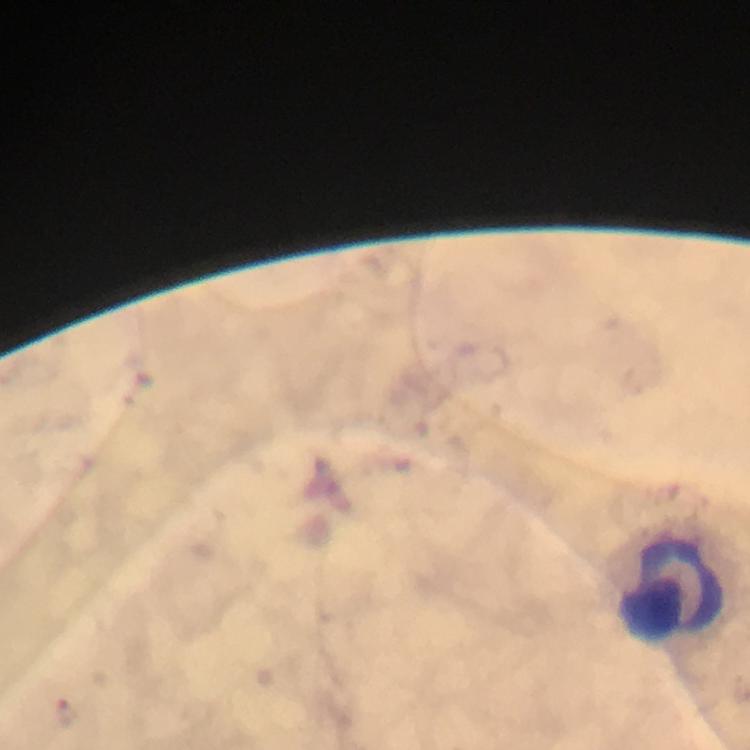

{
  "magnification": "100x",
  "capture": "smartphone camera through the microscope",
  "plasmodium_parasite_locations": "approximate centers as {x, y} in pixels: {69, 713}",
  "immersion_oil": "applied",
  "stain": "Giemsa",
  "preparation": "thick smear",
  "context": "from a diagnostic examination for malaria",
  "image_size": "750×750 pixels",
  "leukocyte_locations": "approximate centers as {x, y} in pixels: {672, 592}",
  "cropped_from": "a single field of view"
}